Identify the parasite.
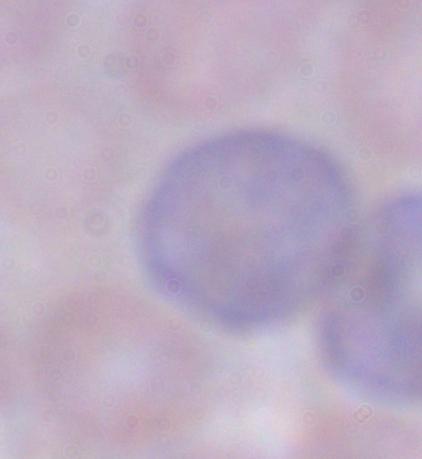

This is a trypanosome.

Captured at 1000x magnification. Micrograph.